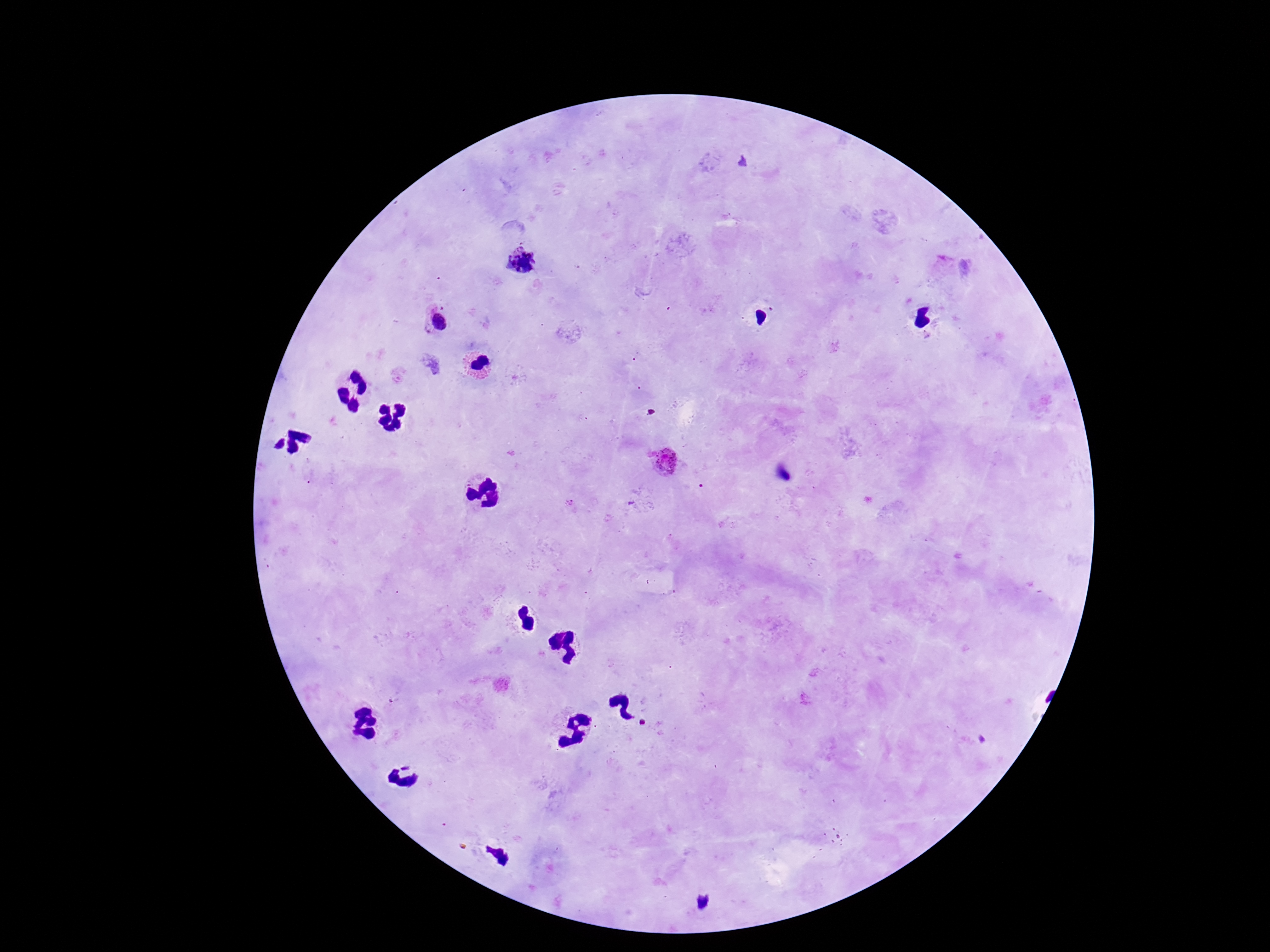

Approximate object centers, in pixels from the top-left corner. Plasmodium parasite locations: (x=521, y=260), (x=437, y=320), (x=663, y=460). Smartphone photograph taken through the microscope eyepiece. Image is 1270×952 pixels. Patient malaria status: infected. 100x magnification. Giemsa-stained preparation. Single field of view. Thick peripheral-blood smear.